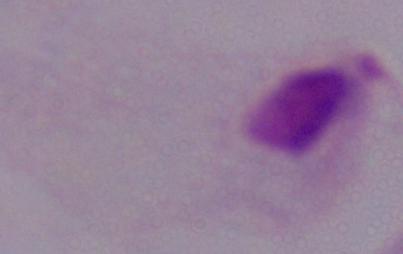

Summary:
  - Magnification: 1000x
  - Modality: micrograph
  - Identification: trichomonad